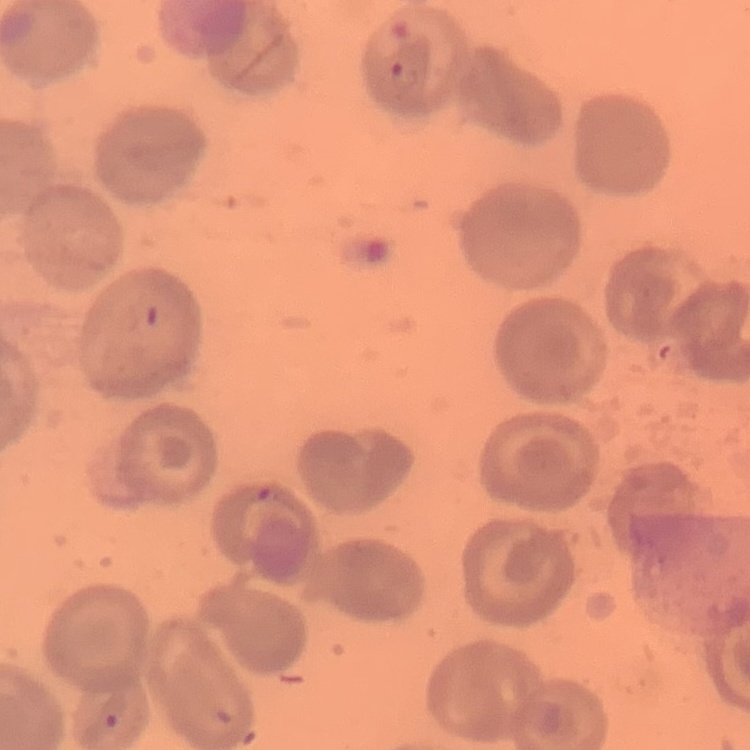

{
  "red_blood_cell_morphology": "no rouleaux formation",
  "image_type": "one tile cut from a larger photomicrograph",
  "stain": "Field's or Giemsa",
  "preparation": "thin blood film"
}